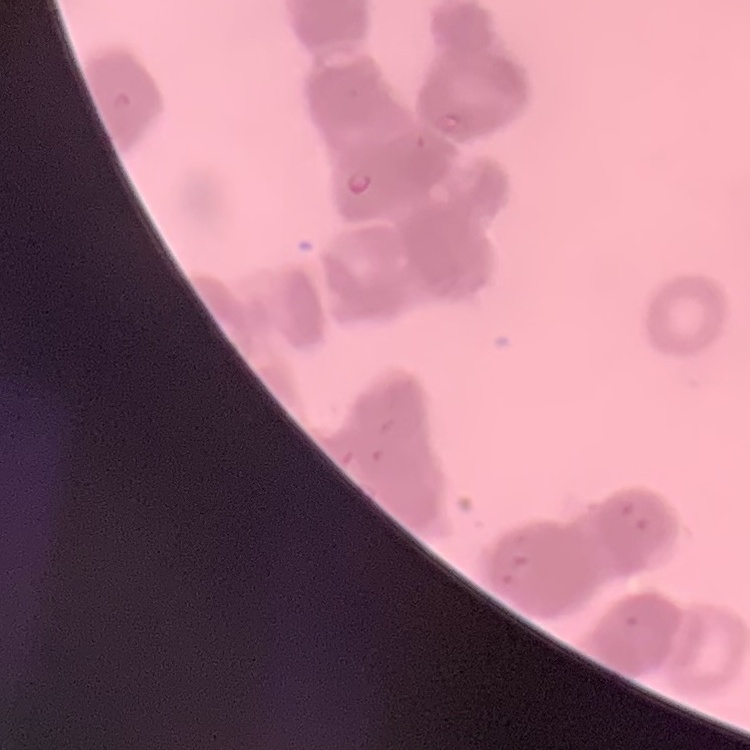
erythrocyte morphology = rouleaux formation
stain = Field's or Giemsa
image type = square crop of a larger photomicrograph
preparation = thin blood film